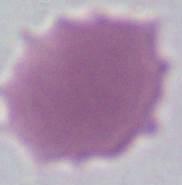

identification: erythrocyte
modality: photomicrograph
magnification: 1000x